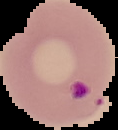
Summary:
  - Malaria status: parasitized
  - Image size: 118×130 pixels
  - Image type: segmented cell region with the area outside set to black
  - Preparation: thin blood smear